State the preparation type.
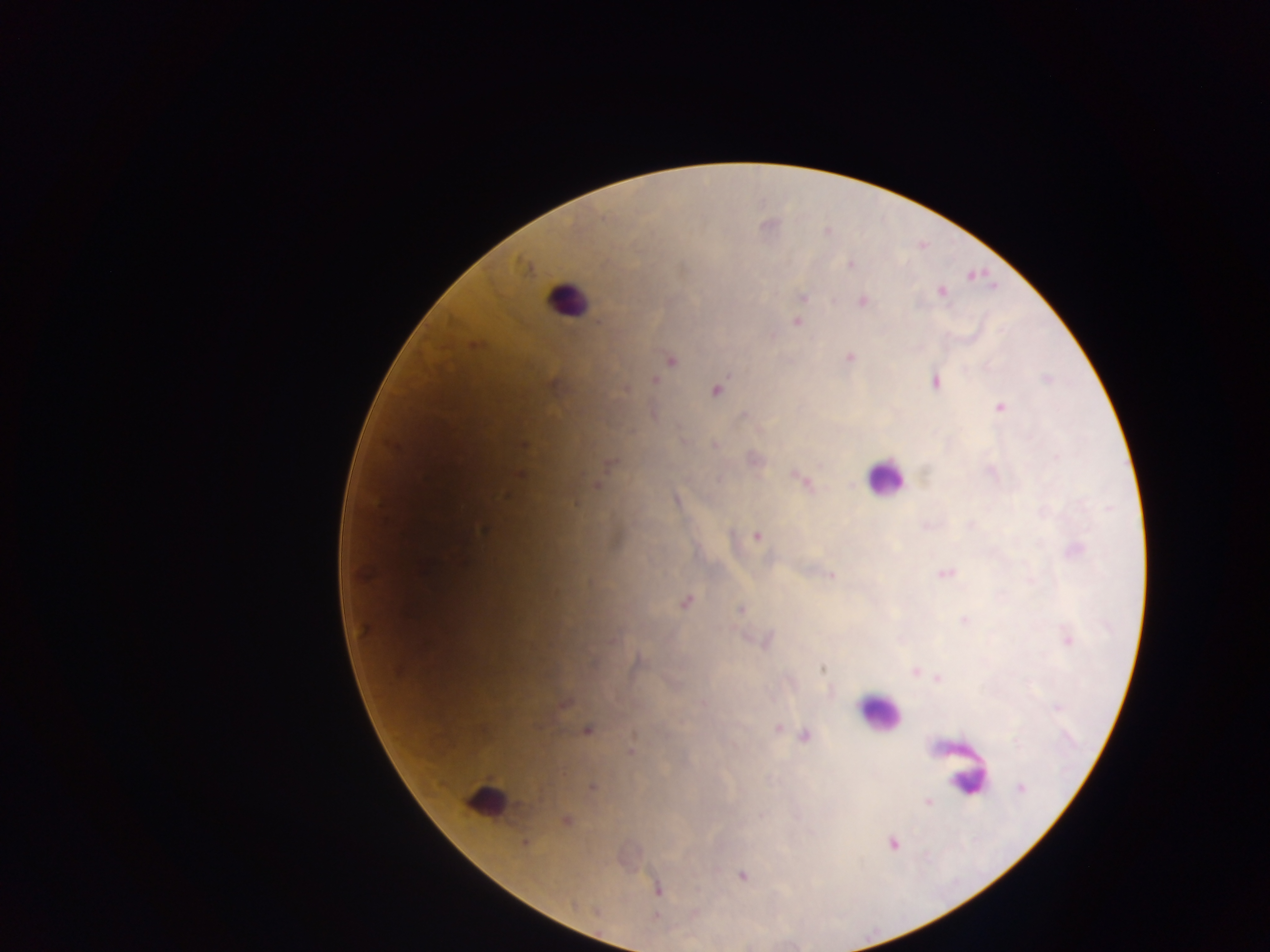

Thick blood film.

Approximate centers as x y in pixels. Plasmodium parasite locations: 827 232; 850 265; 941 292; 803 297; 863 301; 797 322; 850 357; 671 360; 1048 378; 655 380; 935 382; 625 389; 716 390; 999 407; 524 445; 715 445; 610 462; 521 474; 800 480; 597 484; 506 494; 676 500; 484 530; 756 535; 946 572; 831 575; 685 602; 741 609; 964 620; 364 630; 1069 640; 765 642; 822 668; 916 672; 937 678; 564 704; 778 728; 588 731; 806 736; 630 752; 592 786; 1020 788; 927 802; 566 820; 525 844; 892 844; 742 876; 658 889. Leukocyte locations: 566 298; 884 477; 878 713; 968 780; 486 800. Sample from Ghana. One field of view. Image is 1270×952 pixels. Mobile-phone photograph taken through the microscope.